Identify the blood parasite species.
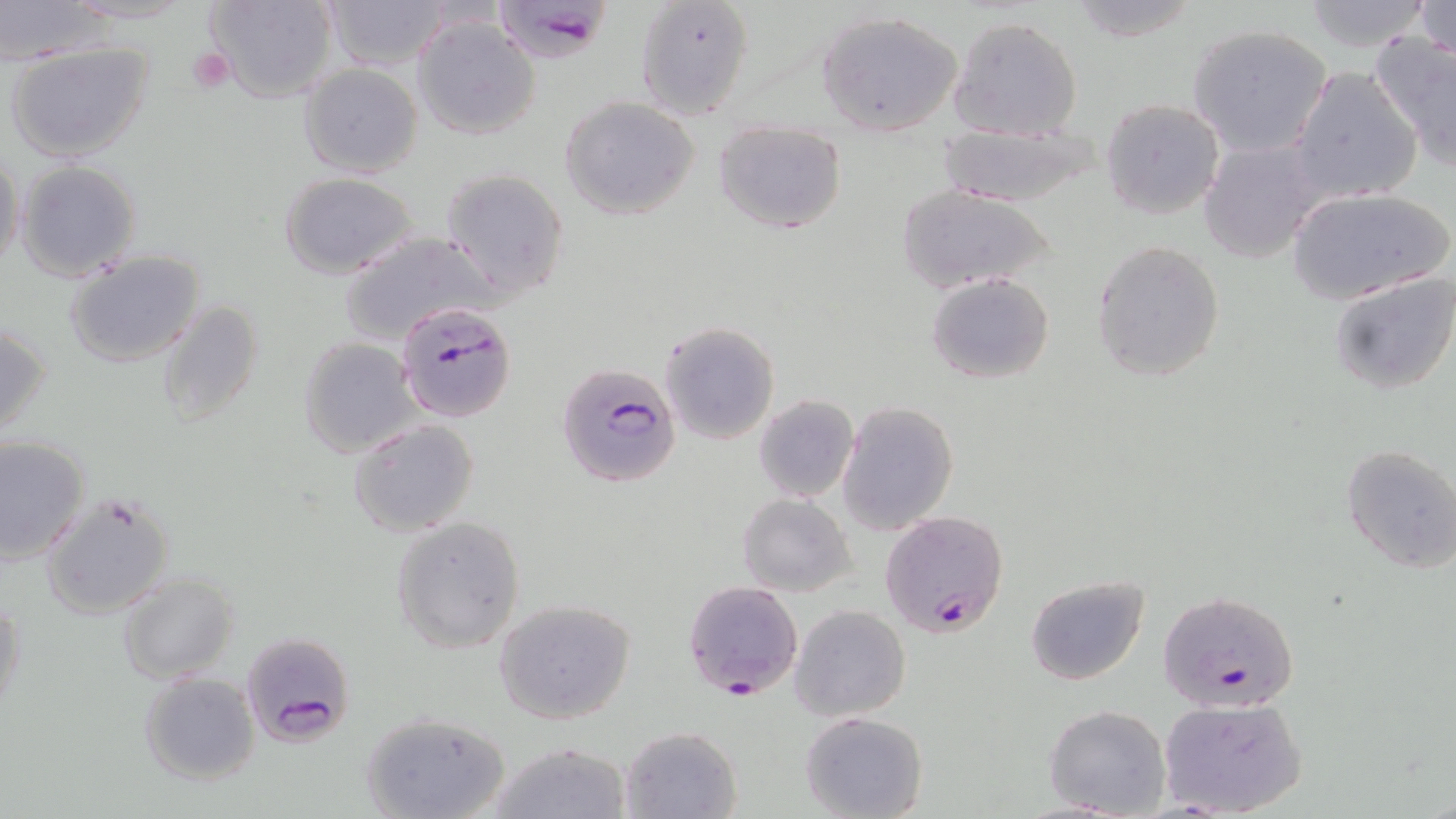
Plasmodium falciparum.

Summary:
  - Coordinate format: approximate bounding boxes as (x1, y1, x2, y2) in pixels
  - Platelet locations: (187, 46, 235, 93)
  - Uninfected red blood cell locations: (205, 0, 336, 104), (326, 0, 449, 69), (636, 0, 755, 122), (1297, 0, 1437, 52), (1411, 0, 1455, 62), (0, 1, 113, 63), (1063, 1, 1207, 44), (818, 10, 964, 137), (413, 15, 541, 140), (947, 15, 1084, 141), (1188, 24, 1333, 158), (1369, 31, 1456, 171), (6, 42, 154, 164), (299, 63, 423, 177), (1289, 67, 1421, 202), (559, 95, 700, 221), (1100, 100, 1225, 221), (714, 120, 846, 234), (931, 121, 1113, 207), (1198, 138, 1327, 265), (0, 150, 25, 273), (15, 160, 142, 281), (438, 168, 571, 300), (279, 172, 419, 279), (896, 184, 1055, 292), (1287, 188, 1452, 300), (339, 229, 497, 344), (1090, 239, 1225, 383), (65, 250, 205, 367), (1328, 270, 1456, 395), (926, 272, 1055, 384), (156, 300, 264, 426), (659, 321, 779, 444), (0, 323, 51, 441), (298, 337, 418, 458), (753, 395, 859, 503), (839, 401, 959, 534), (350, 419, 480, 537), (0, 435, 90, 564), (1340, 444, 1456, 575), (40, 492, 176, 620), (738, 493, 856, 597), (391, 515, 526, 653), (116, 571, 238, 683), (1025, 576, 1148, 686), (0, 596, 26, 719), (493, 598, 634, 723), (789, 603, 911, 721), (139, 672, 260, 785), (1157, 696, 1307, 817), (1044, 704, 1170, 818), (360, 710, 511, 819), (799, 711, 927, 819), (620, 725, 741, 818), (485, 741, 634, 819)
  - Plasmodium falciparum-infected red blood cell locations: (490, 0, 615, 64), (397, 301, 516, 423), (557, 362, 684, 490), (879, 509, 1009, 638), (683, 579, 803, 700), (1156, 589, 1301, 713), (240, 632, 355, 747)
  - Field of view: single
  - Preparation: thin blood smear
  - Stain: May-Grünwald-Giemsa
  - Image size: 1456×819 pixels
  - Magnification: 1000x
  - Modality: optical microscopy